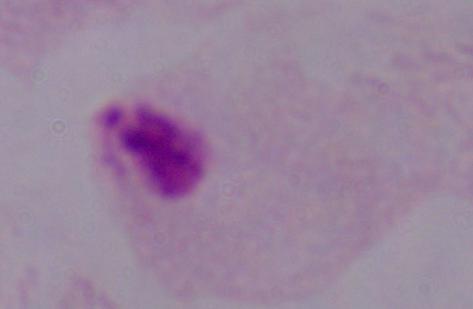
Summary:
  - Magnification: 1000x
  - Modality: micrograph
  - Identification: trichomonad